Assess this cell for malaria.
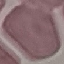
Uninfected.

Summary:
  - Image type: automatically extracted cell patch, resized to 64 × 64 pixels
  - Preparation: thin blood film
  - Capture: smartphone camera at the microscope eyepiece
  - Stain: Giemsa